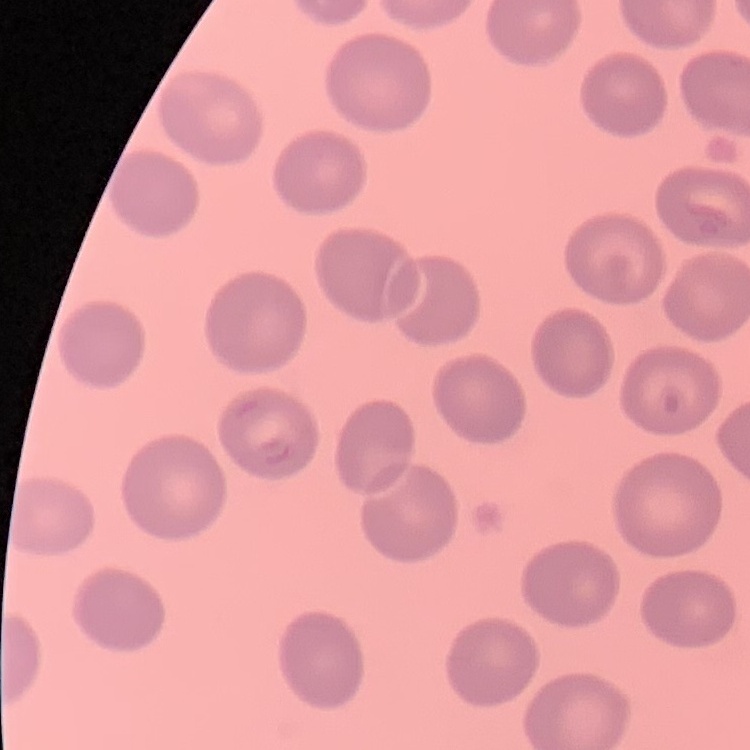

The erythrocytes exhibit no rouleaux formation. Field's or Giemsa stain. Thin blood film. One tile cut from a larger photomicrograph.